Locate every Plasmodium parasite by life-cycle stage, and every leukocyte.
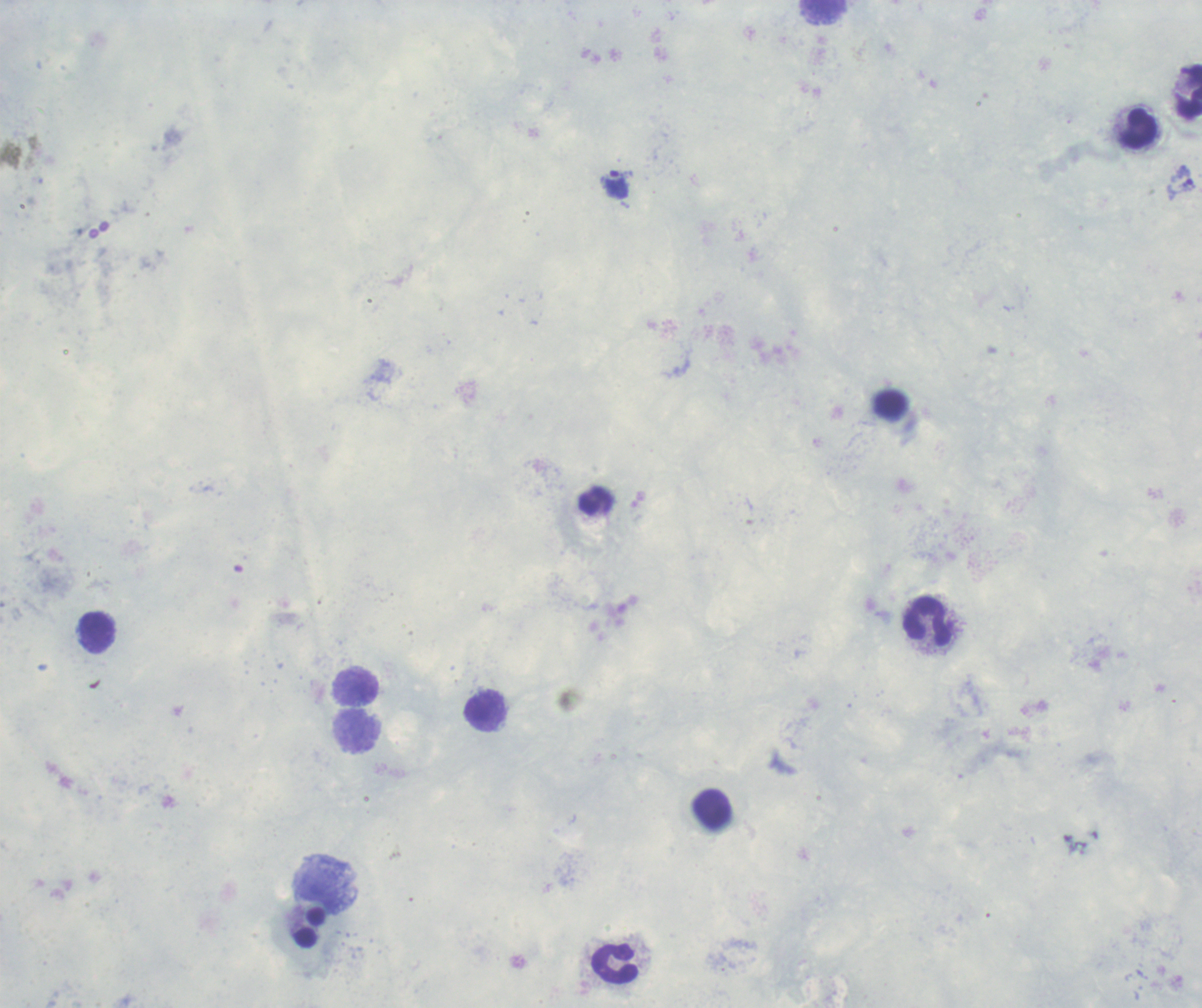

Approximate object centers, in pixels from the top-left corner.
Trophozoites: (x=1181, y=179), (x=615, y=184).
No schizont or gametocyte forms observed.
Leukocytes: (x=824, y=12), (x=1188, y=92), (x=1140, y=130), (x=596, y=500), (x=927, y=622), (x=96, y=633), (x=355, y=687), (x=484, y=706), (x=357, y=731), (x=712, y=808), (x=309, y=927), (x=615, y=963).

image_size: 1202×1008 pixels
stain: Romanowsky
preparation: thick blood smear
context: previously used in an actual diagnosis
magnification: 100x
coloration_quality: good
background_quality: poor
field_of_view: one from this slide